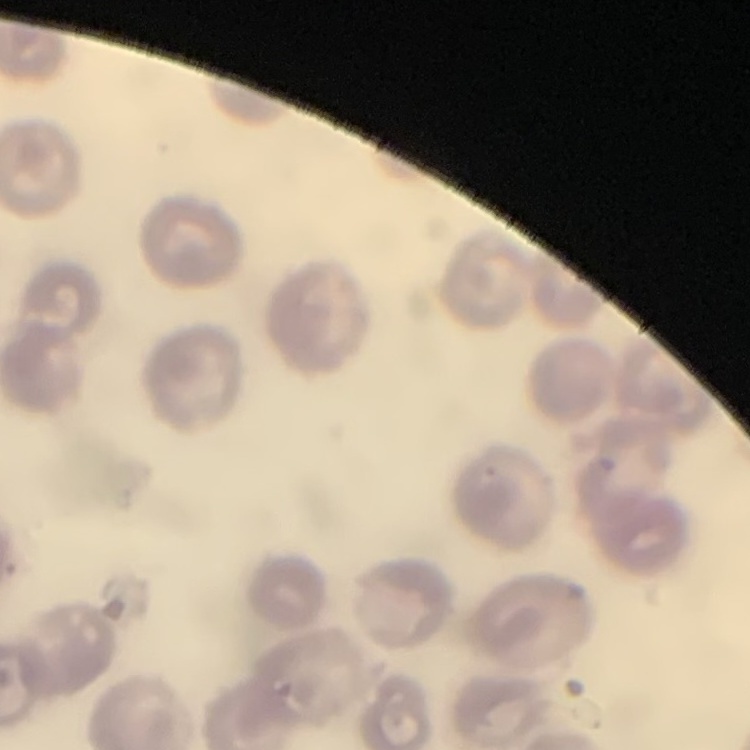

Summary:
  - Erythrocyte morphology: no rouleaux formation
  - Preparation: thin blood film
  - Image type: one tile cut from a larger photomicrograph
  - Stain: Field's or Giemsa